State which parasite is depicted.
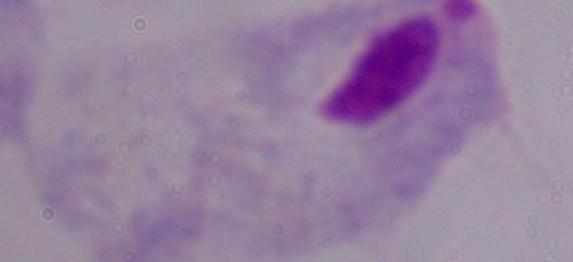
A trichomonad.

magnification: 1000x
modality: micrograph